Identify the preparation type.
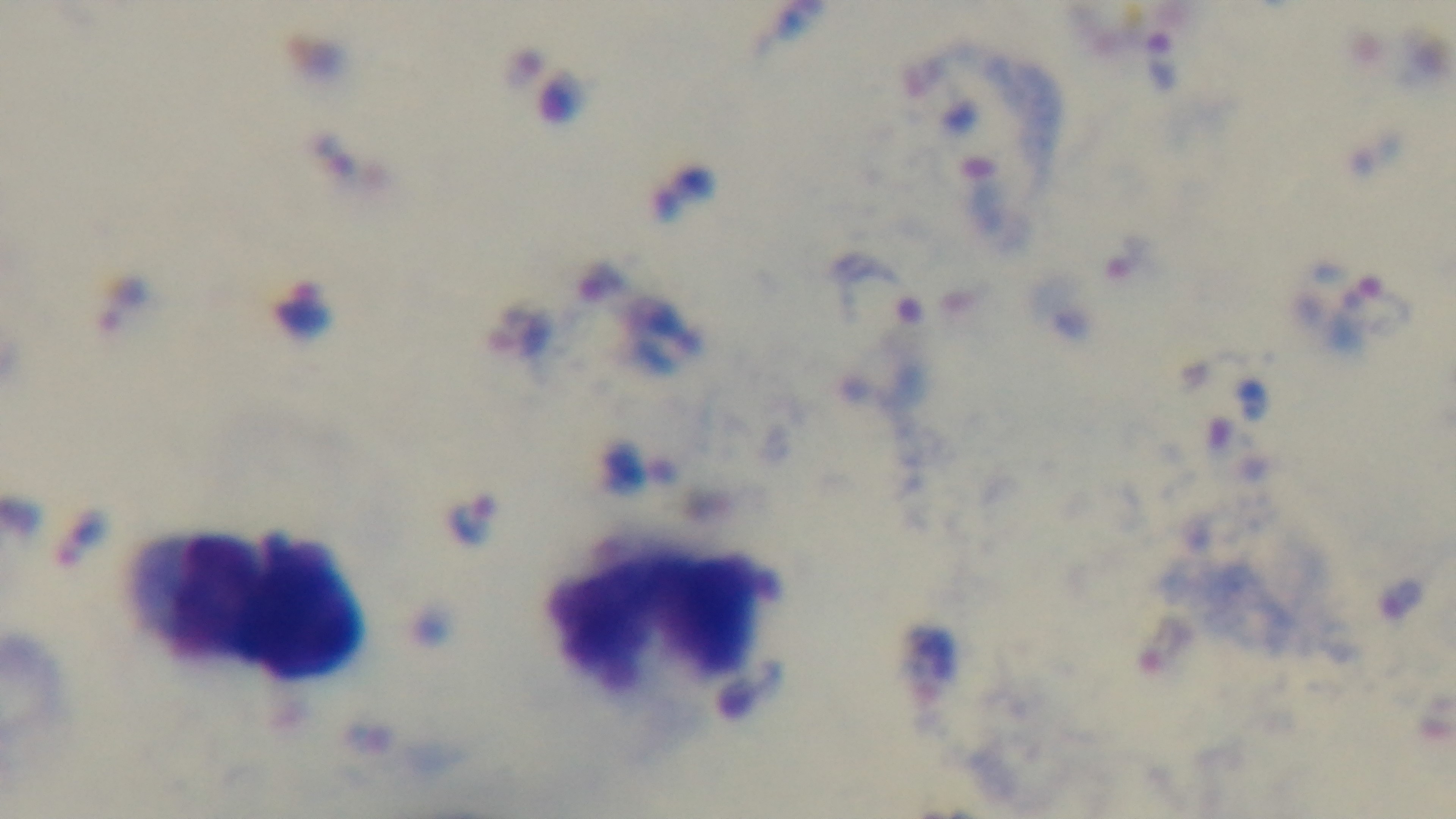
A thick smear.

modality = light microscopy
field of view = one from the slide
objective = 100x oil immersion
capture = mounted 4K digital camera
stain = Giemsa
malaria status = infected